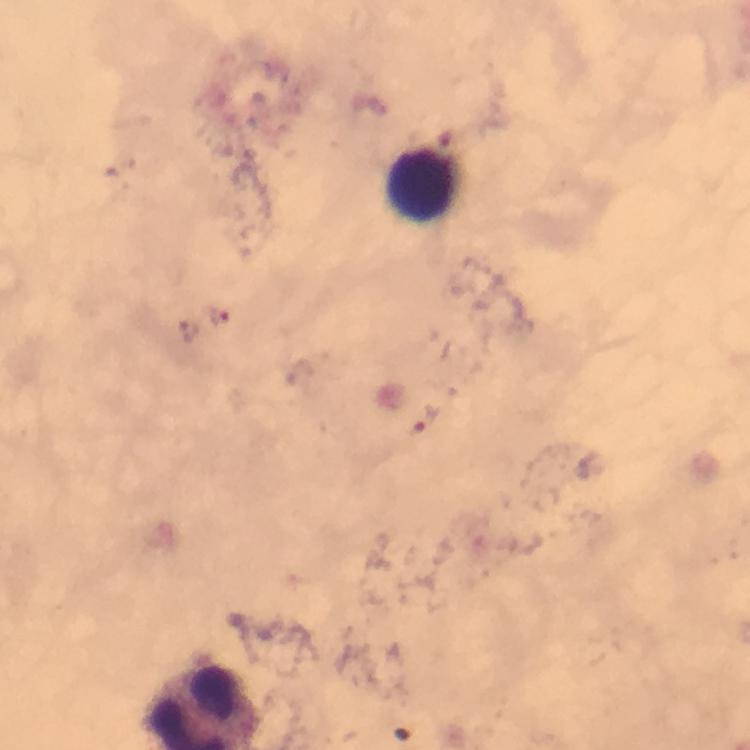

Approximate centers as [x, y] in pixels. Leukocyte locations: [420, 182]. Plasmodium parasite locations: [221, 316], [189, 330]. From a malaria diagnostic workup. Image is 750×750 pixels. Giemsa stain. 100x magnification. Immersion oil applied. Cropped region of a single field of view. Thick smear. Smartphone photograph taken through a microscope.